Locate every uninfected red blood cell.
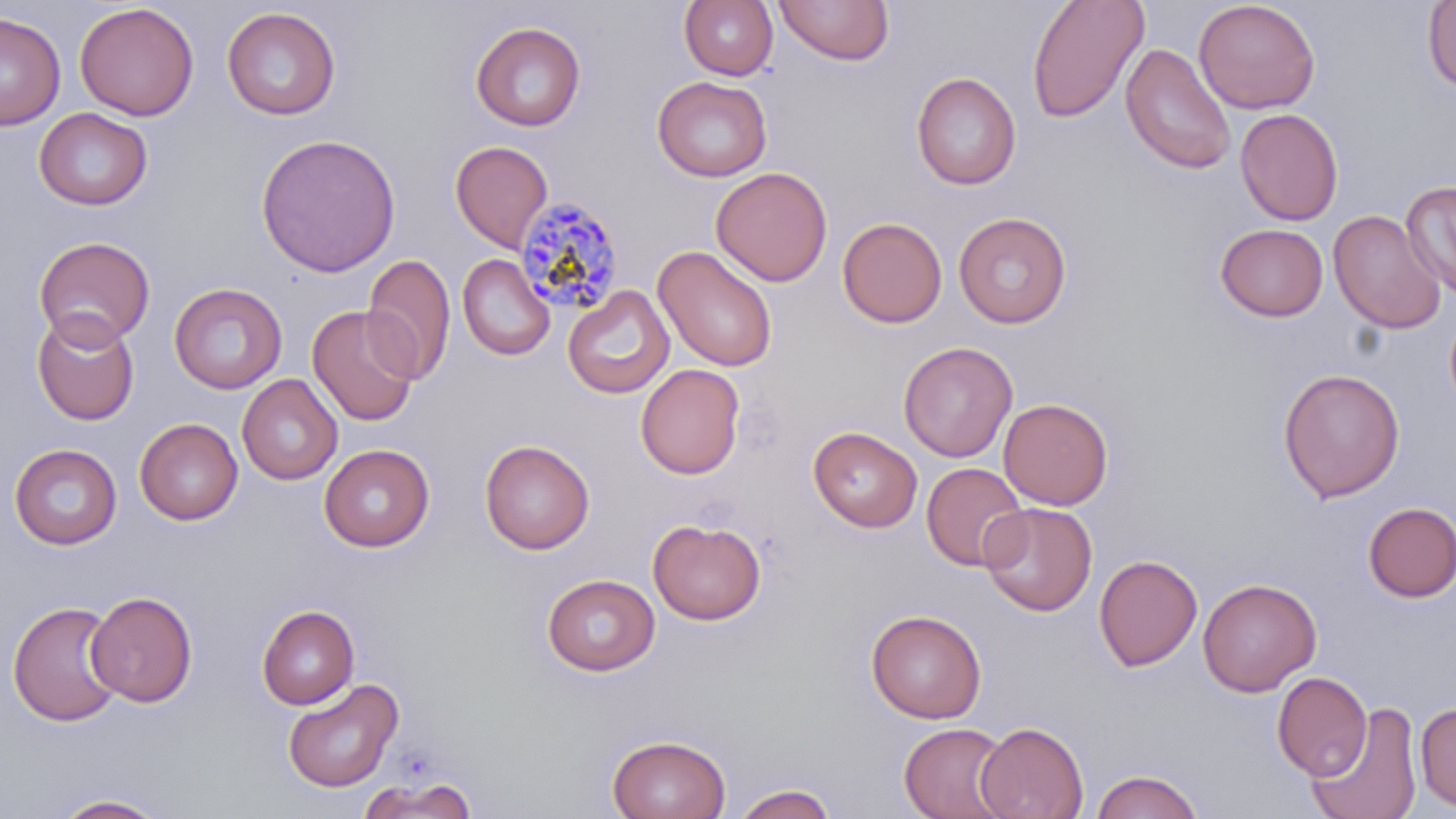
Approximate bounding boxes as (x1, y1, x2, y2) in pixels.
Uninfected red blood cells: (679, 0, 778, 80), (1026, 0, 1149, 123), (1194, 0, 1320, 115), (774, 1, 894, 66), (1422, 1, 1455, 92), (75, 3, 199, 121), (221, 7, 341, 120), (0, 11, 65, 129), (471, 22, 586, 131), (1120, 43, 1237, 175), (911, 71, 1021, 190), (652, 75, 772, 182), (34, 107, 153, 210), (1235, 108, 1343, 226), (255, 133, 401, 277), (450, 140, 553, 252), (710, 166, 832, 287), (1400, 180, 1456, 300), (1328, 210, 1446, 334), (953, 211, 1072, 328), (837, 217, 947, 328), (1215, 223, 1328, 321), (34, 236, 155, 348), (653, 244, 778, 371), (362, 252, 456, 385), (457, 254, 555, 361), (168, 282, 288, 394), (562, 285, 675, 399), (306, 304, 421, 427), (1444, 304, 1456, 416), (32, 312, 140, 426), (899, 341, 1017, 462), (635, 363, 745, 479), (1278, 368, 1405, 502), (237, 374, 343, 485), (998, 398, 1113, 510), (134, 417, 242, 525), (809, 426, 922, 532), (480, 439, 594, 554), (9, 443, 122, 549), (319, 444, 434, 551), (921, 462, 1029, 571), (979, 501, 1097, 617), (1361, 502, 1456, 602), (648, 518, 766, 625), (1094, 553, 1203, 672), (541, 573, 661, 676), (1197, 578, 1321, 697), (85, 591, 198, 707), (7, 600, 125, 727), (257, 605, 360, 709), (866, 609, 986, 723), (1272, 671, 1372, 780), (282, 677, 403, 792), (1415, 701, 1456, 812), (1307, 702, 1421, 819), (974, 721, 1089, 818), (898, 722, 1015, 819), (607, 734, 731, 819), (1090, 769, 1204, 819), (357, 775, 479, 818), (731, 783, 837, 819), (52, 793, 169, 818).

Summary:
  - Plasmodium malariae-infected red blood cell locations: (514, 195, 626, 317)
  - Slide-level diagnosis: Plasmodium malariae
  - Field of view: single
  - Modality: light microscopy
  - Image size: 1456×819 pixels
  - Stain: May-Grünwald-Giemsa
  - Magnification: 1000x
  - Preparation: thin blood smear